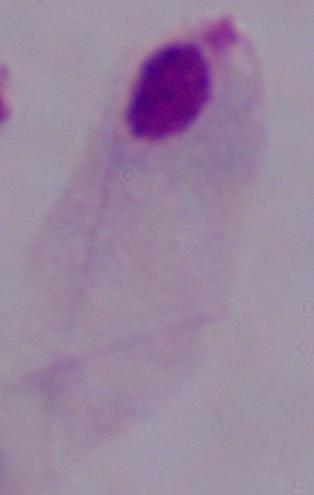
Summary:
  - Magnification: 1000x
  - Identification: trichomonad
  - Modality: photomicrograph